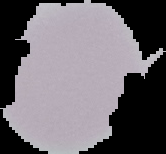
Summary:
  - Result: no Plasmodium parasites seen
  - Image size: 166×154 pixels
  - Image type: segmented cell region with the area outside set to black
  - Preparation: thin blood film